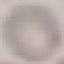
{
  "malaria_status": "uninfected",
  "preparation": "thin blood smear",
  "capture": "smartphone through the microscope eyepiece",
  "stain": "Giemsa",
  "image_type": "cell patch, automatically extracted from a larger field of view and resized to 64 × 64 pixels"
}